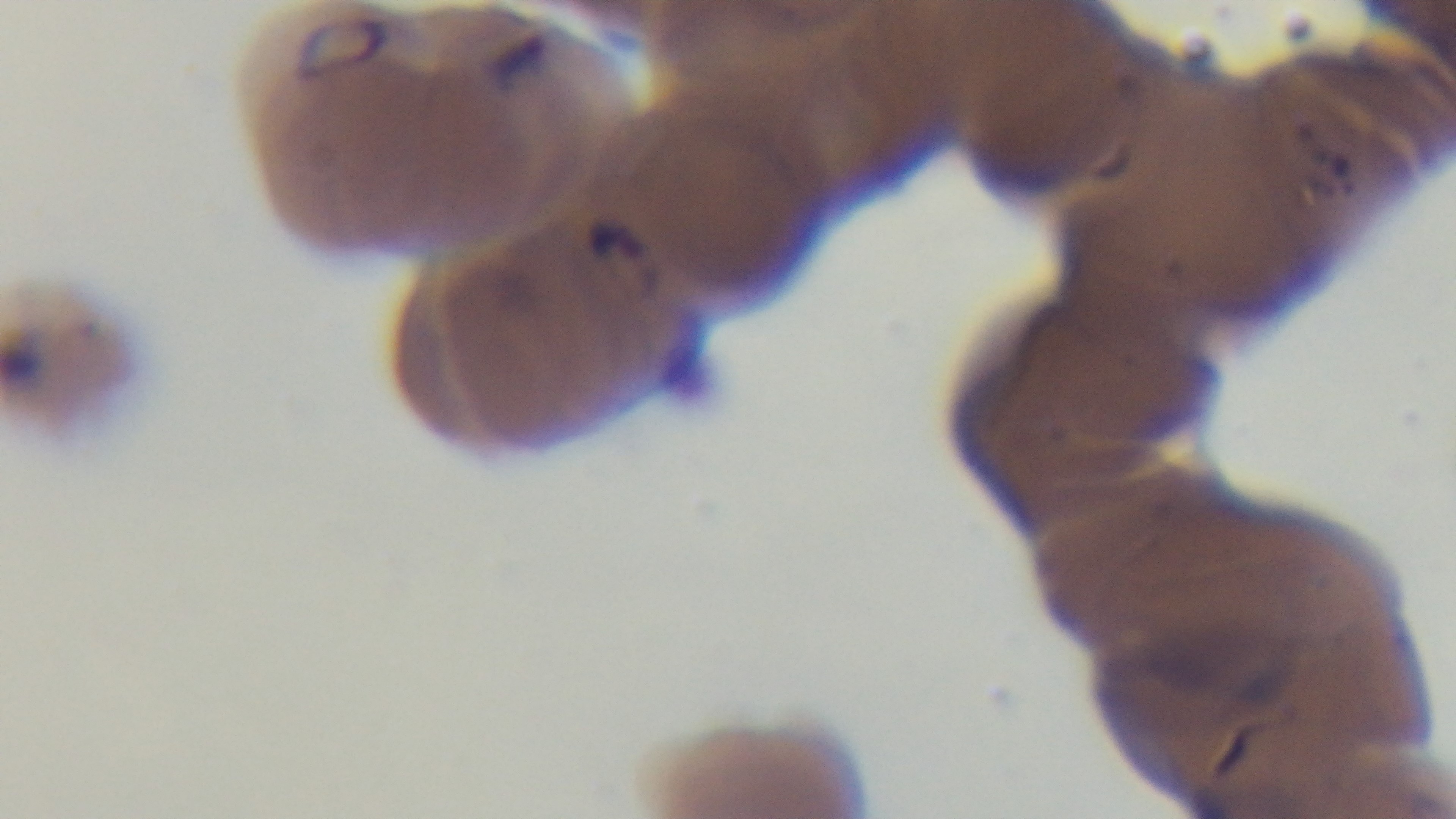

Summary:
  - Preparation: thin blood film
  - Field of view: one from the slide
  - Modality: light microscopy
  - Capture: mounted 4K digital camera
  - Stain: Giemsa
  - Malaria status: infected
  - Objective: 100x oil immersion